Find the cells and give the type of each one.
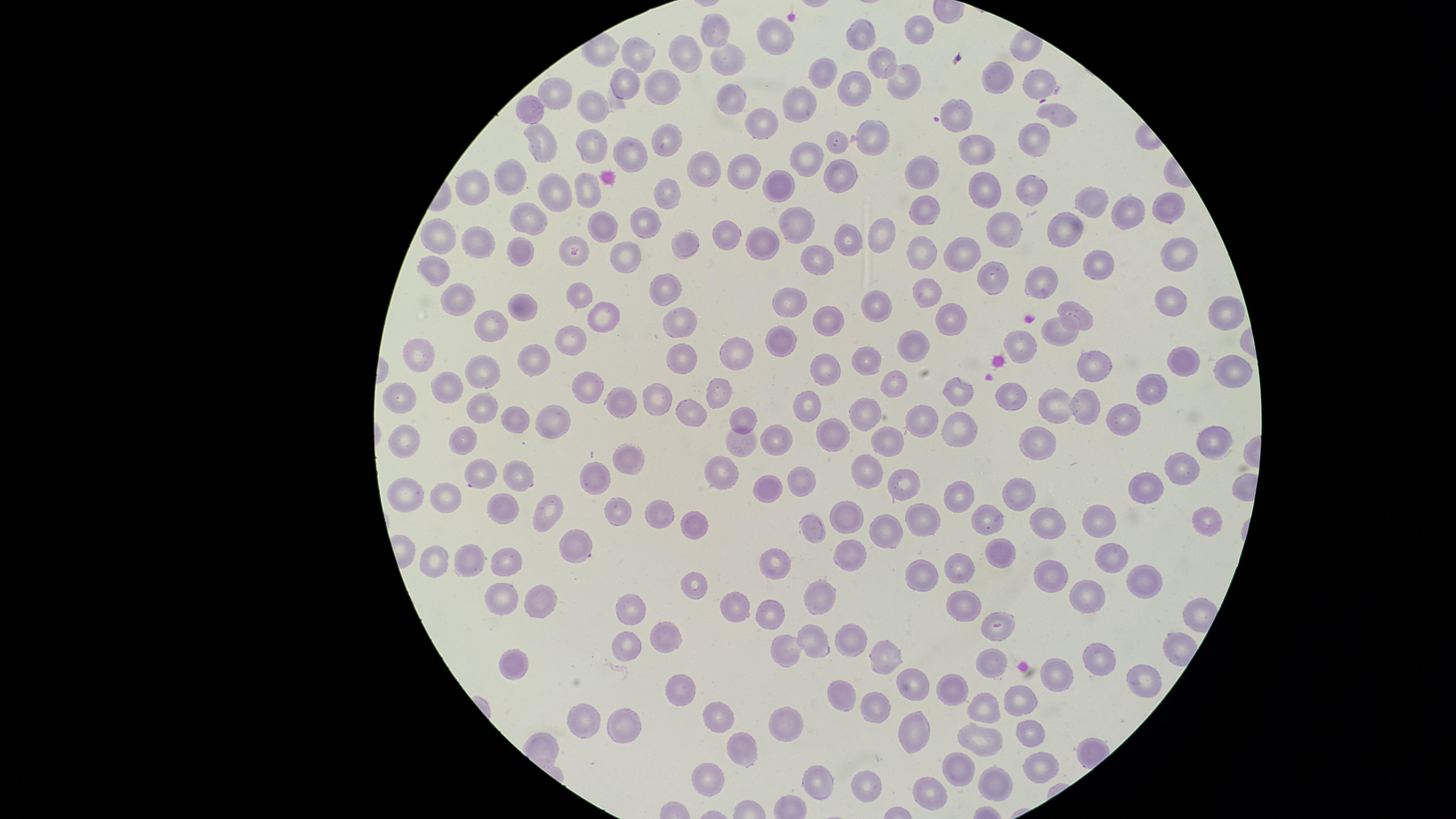

Approximate marker points as [x, y] in pixels.
Parasitized red blood cells: [575, 251], [999, 626].
Uninfected red blood cells: [718, 29], [923, 29], [778, 34], [865, 34], [686, 49], [640, 56], [732, 59], [880, 65], [824, 73], [996, 75], [902, 80], [1039, 81], [627, 84], [856, 87], [662, 91], [555, 92], [734, 96], [802, 102], [598, 105], [528, 109], [960, 114], [1057, 114], [765, 123], [1032, 137], [663, 138], [873, 138], [540, 139], [841, 140], [587, 145], [979, 146], [631, 151], [814, 151], [703, 168], [746, 168], [839, 170], [928, 171], [504, 179], [777, 186], [983, 186], [472, 187], [1029, 189], [585, 190], [668, 194], [555, 197], [1092, 201], [927, 208], [1159, 208], [1127, 209], [532, 214], [649, 219], [1011, 222], [801, 226], [1067, 227], [722, 230], [876, 233], [847, 238], [443, 239], [761, 240], [477, 241], [682, 243], [967, 248], [924, 249], [1181, 249], [632, 250], [522, 251], [815, 257], [1104, 257], [435, 270], [1043, 280], [994, 282], [671, 290], [929, 290], [582, 292], [459, 301], [1163, 302], [794, 303], [879, 306], [523, 308], [1225, 311], [1079, 313], [830, 316], [949, 316], [607, 317], [681, 321], [493, 322], [1055, 331], [783, 338], [573, 340], [1023, 343], [913, 348], [738, 351], [423, 356], [542, 356], [688, 357], [866, 357], [1097, 358], [1177, 358], [1234, 369], [827, 370], [488, 371], [591, 385], [893, 385], [1155, 385], [450, 389], [962, 391], [1010, 391], [718, 392], [621, 395], [405, 396], [1083, 402], [486, 405], [656, 405], [812, 405], [1050, 406], [692, 409], [561, 411], [875, 414], [1123, 417], [928, 418], [518, 421], [749, 421], [960, 426], [461, 432], [403, 437], [780, 437], [830, 437], [1210, 440], [743, 441], [1043, 443], [886, 445], [631, 454], [866, 467], [1184, 468], [724, 470], [483, 476], [519, 478], [805, 478], [592, 479], [904, 487], [770, 488], [1151, 488], [1021, 493], [403, 499], [965, 500], [447, 502], [505, 510], [548, 510], [617, 511], [658, 515], [849, 516], [1104, 519], [1204, 520], [924, 522], [1050, 522], [820, 524], [991, 525], [698, 526], [886, 528], [578, 543], [1006, 547], [846, 555], [441, 557], [469, 558], [1108, 559], [777, 562], [508, 563], [956, 567], [926, 575], [1054, 580], [1148, 580], [698, 586], [502, 597], [820, 597], [1089, 597], [542, 601], [739, 601], [961, 604], [630, 607], [772, 613], [669, 630], [816, 639], [625, 641], [844, 641], [889, 653], [788, 654], [1100, 659], [994, 664], [519, 666], [1062, 671], [1138, 680], [910, 687], [953, 688], [678, 690], [842, 697], [1028, 703], [877, 709], [986, 714], [716, 716], [583, 718], [786, 722], [631, 728], [1032, 733], [911, 735], [985, 739], [742, 749], [1040, 771], [962, 772], [712, 778], [870, 782], [818, 783], [992, 784], [930, 792].
No white blood cells identified.

Summary:
  - Species: Plasmodium falciparum
  - Capture: smartphone photograph through the microscope eyepiece
  - Stain: Giemsa
  - Preparation: thin smear of blood
  - Image size: 1456×819 pixels
  - Visible region: circular
  - Field of view: single